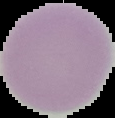

Summary:
  - Malaria status: uninfected
  - Image type: cell region segmented out of the field of view; surrounding area masked to black
  - Preparation: thin blood smear
  - Image size: 115×118 pixels